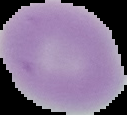 Result: no Plasmodium parasites seen. From a thin blood film. Segmented cell region on a black background. Image is 127×115 pixels.